Report the malaria status of this cell.
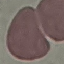
It is uninfected.

Summary:
  - Capture: smartphone through the microscope eyepiece
  - Image type: automatically extracted cell patch, resized to 64 × 64 pixels
  - Preparation: thin smear
  - Stain: Giemsa